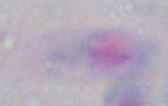

Summary:
  - Modality: micrograph
  - Identification: Toxoplasma gondii
  - Magnification: 1000x